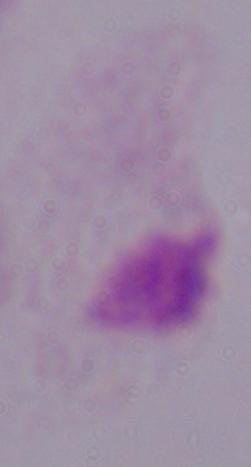

Captured at 1000x magnification. A trichomonad is seen. Photomicrograph.